Give the extent of all Plasmodium falciparum-infected red blood cells.
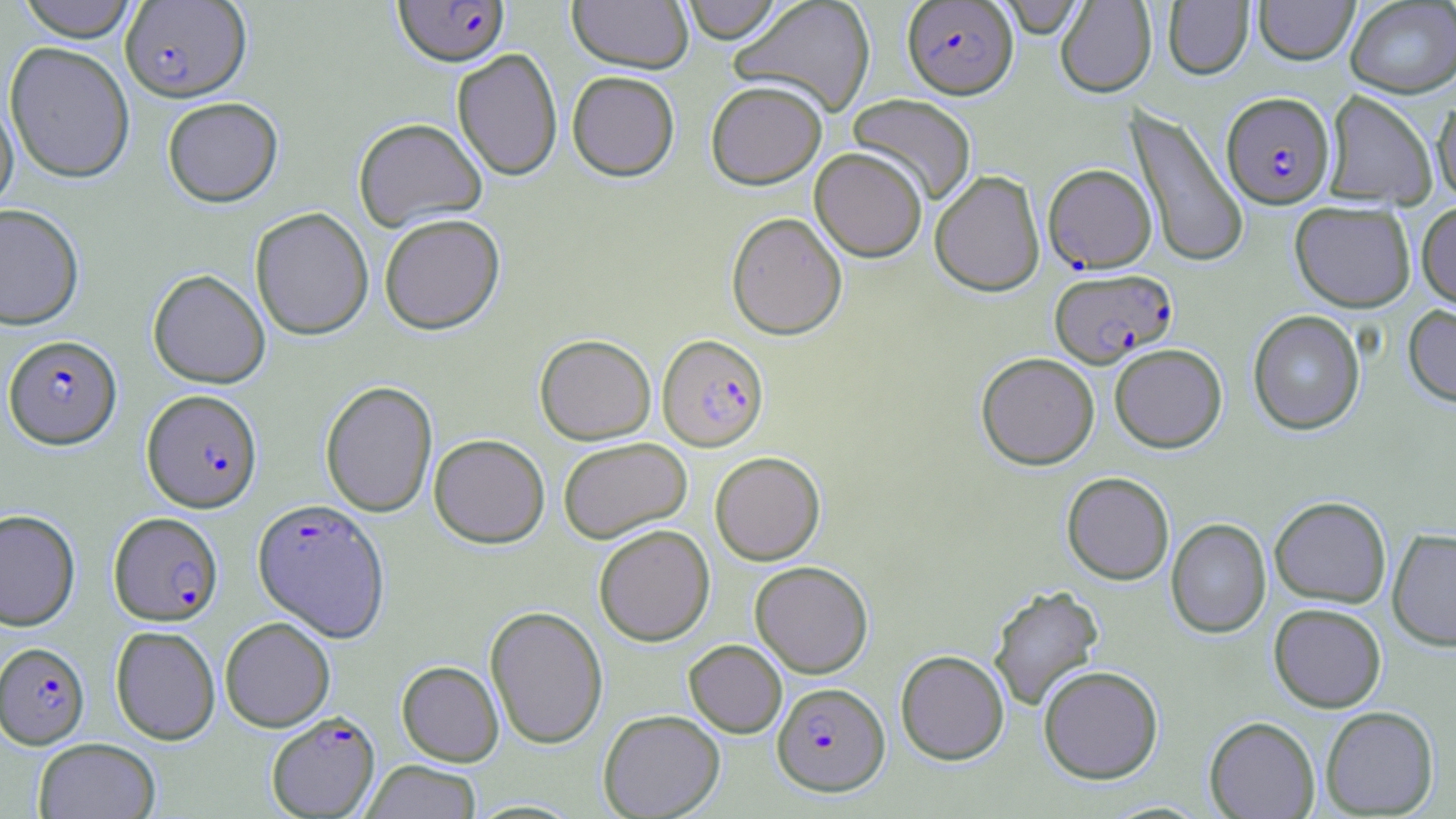

Approximate bounding boxes as [x1, y1, x2, y2] in pixels.
Plasmodium falciparum-infected red blood cells: [120, 1, 252, 102], [393, 1, 510, 67], [902, 1, 1018, 99], [1222, 91, 1335, 208], [1050, 166, 1163, 276], [1049, 268, 1177, 367], [657, 333, 769, 451], [3, 335, 121, 450], [142, 389, 262, 512], [252, 499, 389, 641], [109, 511, 223, 625], [0, 642, 90, 749], [772, 681, 890, 796], [266, 711, 380, 818].

slide-level diagnosis = Plasmodium falciparum
stain = May-Grünwald-Giemsa
field of view = one of a larger specimen
uninfected red blood cell locations = approximate bounding boxes as [x1, y1, x2, y2] in pixels: [15, 0, 140, 42], [567, 0, 693, 73], [680, 0, 783, 44], [729, 0, 877, 116], [996, 0, 1087, 39], [1055, 0, 1156, 97], [1254, 0, 1359, 65], [1163, 1, 1253, 79], [1345, 1, 1456, 98], [4, 41, 135, 184], [452, 48, 563, 180], [567, 71, 680, 181], [706, 80, 827, 189], [1323, 90, 1437, 209], [847, 93, 977, 205], [0, 94, 18, 216], [1432, 95, 1456, 203], [162, 96, 283, 207], [1126, 106, 1248, 268], [353, 117, 487, 233], [810, 147, 928, 262], [930, 169, 1045, 296], [1290, 201, 1416, 312], [1416, 201, 1456, 310], [0, 204, 84, 330], [250, 207, 374, 340], [726, 211, 848, 340], [379, 213, 505, 334], [148, 269, 270, 388], [1403, 303, 1456, 409], [1247, 309, 1365, 435], [534, 333, 656, 444], [1109, 343, 1227, 452], [976, 352, 1100, 470], [320, 380, 438, 518], [429, 433, 550, 548], [558, 436, 692, 542], [710, 451, 826, 565], [1062, 472, 1174, 585], [1270, 496, 1391, 607], [0, 509, 80, 631], [1166, 518, 1271, 638], [593, 524, 715, 646], [1387, 527, 1456, 651], [750, 561, 873, 678], [988, 585, 1104, 712], [1268, 603, 1387, 712], [485, 605, 608, 749], [220, 616, 335, 731], [110, 625, 220, 744], [684, 639, 787, 738], [895, 649, 1009, 765], [397, 660, 504, 766], [1038, 665, 1163, 783], [1321, 706, 1439, 817], [598, 709, 725, 818], [1204, 716, 1320, 818], [33, 737, 161, 819], [361, 760, 483, 819]
preparation = thin blood film
modality = optical microscopy
magnification = 1000x
image size = 1456×819 pixels